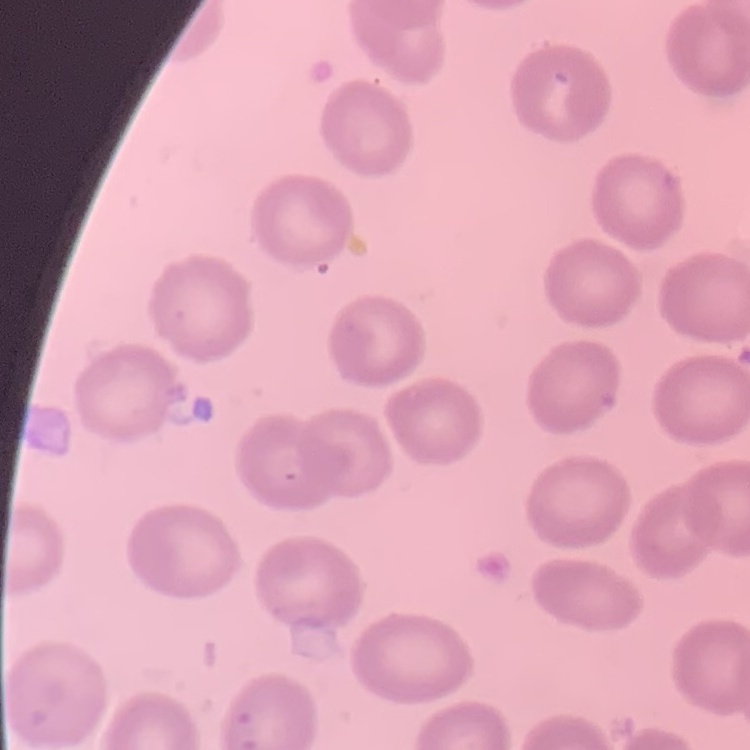 The red blood cells exhibit no rouleaux formation. Thin peripheral smear. Field's or Giemsa stain. Square crop of a larger photomicrograph.